Identify the parasite.
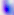
Toxoplasma gondii.

modality = micrograph
magnification = 400x